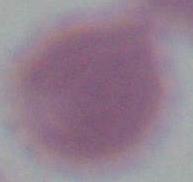
An erythrocyte is seen. Photomicrograph. 1000x magnification.